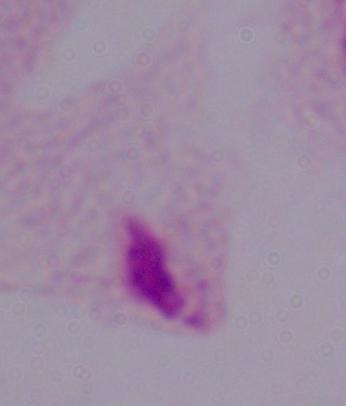

A trichomonad is seen. Captured at 1000x magnification. Micrograph.